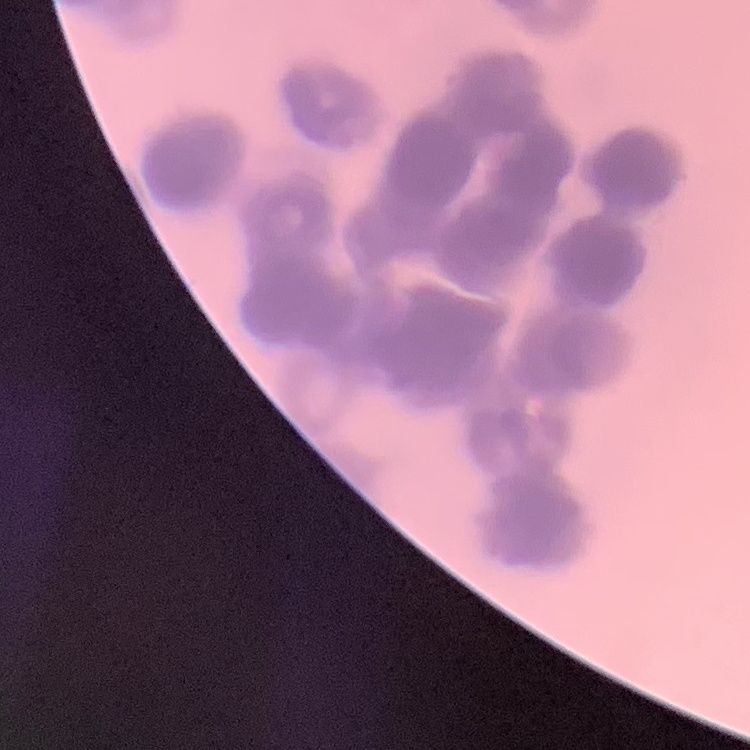

The erythrocytes exhibit rouleaux formation. Field's or Giemsa stain. Thin peripheral smear. Square crop of a larger photomicrograph.